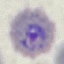
malaria_status: parasitized
image_type: cell patch, automatically extracted from a larger field of view and resized to 64 × 64 pixels
stain: Giemsa
capture: smartphone through the microscope eyepiece
preparation: thin blood smear